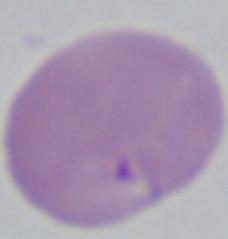

modality = micrograph
magnification = 1000x
identification = Babesia